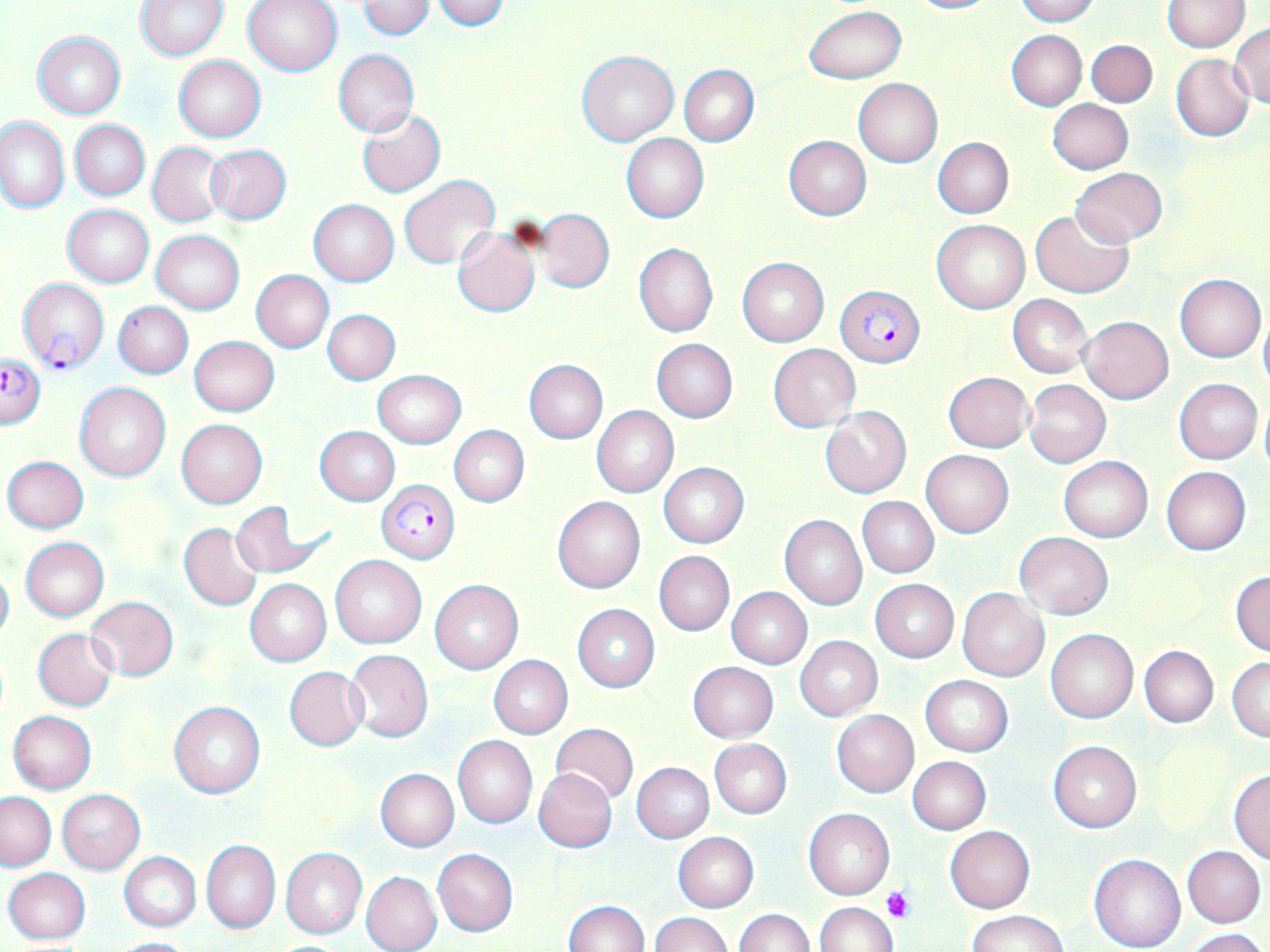 Approximate bounding boxes as named x1/y1/x2/y2 corners in pixels. Uninfected red blood cell locations: (x1=135, y1=0, x2=227, y2=60), (x1=243, y1=0, x2=343, y2=77), (x1=357, y1=0, x2=434, y2=40), (x1=432, y1=0, x2=510, y2=31), (x1=905, y1=0, x2=996, y2=14), (x1=1013, y1=0, x2=1098, y2=25), (x1=1162, y1=1, x2=1248, y2=52), (x1=805, y1=5, x2=905, y2=84), (x1=1230, y1=25, x2=1270, y2=108), (x1=1006, y1=30, x2=1087, y2=110), (x1=32, y1=31, x2=126, y2=119), (x1=1087, y1=39, x2=1157, y2=107), (x1=334, y1=48, x2=419, y2=137), (x1=578, y1=50, x2=679, y2=146), (x1=1170, y1=54, x2=1254, y2=141), (x1=174, y1=55, x2=266, y2=142), (x1=679, y1=65, x2=759, y2=146), (x1=854, y1=79, x2=942, y2=167), (x1=1048, y1=100, x2=1134, y2=174), (x1=357, y1=108, x2=445, y2=197), (x1=1, y1=116, x2=69, y2=212), (x1=70, y1=119, x2=149, y2=201), (x1=620, y1=133, x2=708, y2=223), (x1=783, y1=137, x2=871, y2=220), (x1=932, y1=138, x2=1013, y2=219), (x1=147, y1=142, x2=227, y2=227), (x1=205, y1=145, x2=291, y2=224), (x1=1070, y1=168, x2=1168, y2=245), (x1=399, y1=175, x2=500, y2=269), (x1=309, y1=199, x2=398, y2=286), (x1=62, y1=204, x2=153, y2=287), (x1=1030, y1=208, x2=1133, y2=298), (x1=535, y1=210, x2=614, y2=292), (x1=932, y1=219, x2=1030, y2=314), (x1=451, y1=226, x2=539, y2=317), (x1=150, y1=230, x2=244, y2=314), (x1=633, y1=243, x2=718, y2=337), (x1=737, y1=257, x2=828, y2=346), (x1=250, y1=269, x2=334, y2=352), (x1=1174, y1=273, x2=1266, y2=363), (x1=1008, y1=295, x2=1092, y2=378), (x1=113, y1=301, x2=193, y2=379), (x1=323, y1=309, x2=399, y2=384), (x1=1258, y1=312, x2=1270, y2=393), (x1=1079, y1=316, x2=1174, y2=405), (x1=189, y1=337, x2=278, y2=415), (x1=652, y1=339, x2=737, y2=423), (x1=768, y1=344, x2=860, y2=431), (x1=524, y1=360, x2=607, y2=444), (x1=373, y1=370, x2=465, y2=447), (x1=944, y1=372, x2=1034, y2=452), (x1=1175, y1=378, x2=1262, y2=465), (x1=1025, y1=380, x2=1111, y2=469), (x1=75, y1=383, x2=171, y2=482), (x1=1258, y1=398, x2=1270, y2=480), (x1=592, y1=405, x2=679, y2=498), (x1=821, y1=407, x2=911, y2=498), (x1=176, y1=419, x2=268, y2=509), (x1=315, y1=426, x2=400, y2=506), (x1=449, y1=426, x2=528, y2=506), (x1=921, y1=449, x2=1014, y2=537), (x1=3, y1=456, x2=89, y2=534), (x1=1058, y1=456, x2=1153, y2=542), (x1=658, y1=461, x2=749, y2=547), (x1=1161, y1=466, x2=1250, y2=555), (x1=552, y1=495, x2=645, y2=593), (x1=857, y1=497, x2=938, y2=577), (x1=229, y1=501, x2=322, y2=579), (x1=779, y1=515, x2=867, y2=610), (x1=179, y1=523, x2=263, y2=611), (x1=1014, y1=531, x2=1113, y2=619), (x1=21, y1=537, x2=109, y2=621), (x1=655, y1=551, x2=733, y2=636), (x1=329, y1=554, x2=427, y2=648), (x1=1129, y1=559, x2=1208, y2=635), (x1=0, y1=564, x2=13, y2=644), (x1=1230, y1=570, x2=1270, y2=656), (x1=870, y1=579, x2=958, y2=662), (x1=244, y1=580, x2=331, y2=666), (x1=430, y1=580, x2=523, y2=674), (x1=726, y1=587, x2=811, y2=668), (x1=957, y1=588, x2=1050, y2=681), (x1=85, y1=596, x2=179, y2=681), (x1=572, y1=603, x2=660, y2=692), (x1=33, y1=627, x2=118, y2=711), (x1=1045, y1=628, x2=1138, y2=724), (x1=794, y1=635, x2=883, y2=721), (x1=1139, y1=646, x2=1218, y2=727), (x1=344, y1=649, x2=433, y2=741), (x1=488, y1=656, x2=572, y2=739), (x1=1226, y1=657, x2=1270, y2=741), (x1=687, y1=661, x2=778, y2=743), (x1=283, y1=666, x2=367, y2=750), (x1=920, y1=675, x2=1013, y2=756), (x1=169, y1=702, x2=265, y2=798), (x1=8, y1=710, x2=96, y2=794), (x1=831, y1=710, x2=919, y2=798), (x1=549, y1=723, x2=639, y2=806), (x1=453, y1=735, x2=537, y2=829), (x1=709, y1=739, x2=792, y2=819), (x1=1048, y1=740, x2=1142, y2=833), (x1=1147, y1=741, x2=1230, y2=835), (x1=908, y1=757, x2=991, y2=834), (x1=631, y1=761, x2=714, y2=843), (x1=375, y1=768, x2=459, y2=852), (x1=534, y1=768, x2=617, y2=852), (x1=1228, y1=768, x2=1270, y2=864), (x1=57, y1=789, x2=145, y2=874), (x1=1, y1=792, x2=55, y2=871), (x1=803, y1=807, x2=895, y2=901), (x1=945, y1=825, x2=1035, y2=913), (x1=672, y1=832, x2=759, y2=912), (x1=202, y1=840, x2=280, y2=933), (x1=1183, y1=846, x2=1266, y2=928), (x1=280, y1=847, x2=368, y2=940), (x1=433, y1=848, x2=518, y2=937), (x1=119, y1=852, x2=201, y2=932), (x1=1089, y1=852, x2=1187, y2=952), (x1=3, y1=867, x2=91, y2=944), (x1=361, y1=870, x2=443, y2=952), (x1=563, y1=900, x2=650, y2=951), (x1=814, y1=901, x2=897, y2=952), (x1=734, y1=908, x2=813, y2=952), (x1=968, y1=910, x2=1066, y2=951), (x1=649, y1=913, x2=734, y2=952), (x1=1184, y1=928, x2=1266, y2=952), (x1=109, y1=937, x2=195, y2=951). Plasmodium falciparum-infected red blood cell locations: (x1=20, y1=279, x2=110, y2=375), (x1=836, y1=286, x2=924, y2=364), (x1=0, y1=356, x2=46, y2=428), (x1=378, y1=479, x2=460, y2=563). Platelet locations: (x1=883, y1=887, x2=911, y2=924). Slide-level diagnosis: Plasmodium falciparum. 1000x magnification. Image is 1270×952 pixels. Thin blood smear. Optical microscopy. Single field of view. May-Grünwald-Giemsa stain.